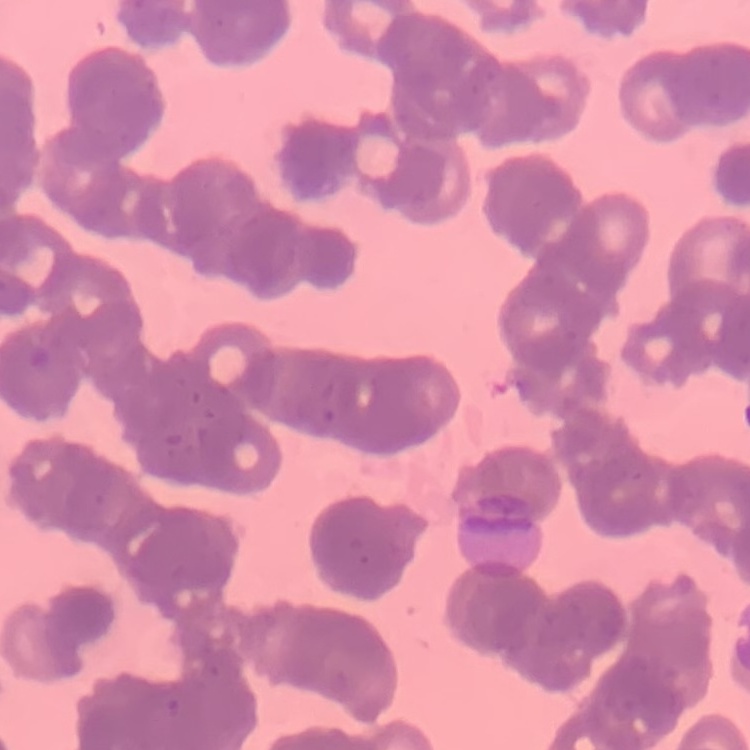

The red blood cells show rouleaux formation. Square crop of a larger photomicrograph. Thin blood smear. Field's or Giemsa stain.